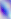 Captured at 400x magnification. Toxoplasma gondii is shown. Photomicrograph.